Point out each Plasmodium parasite.
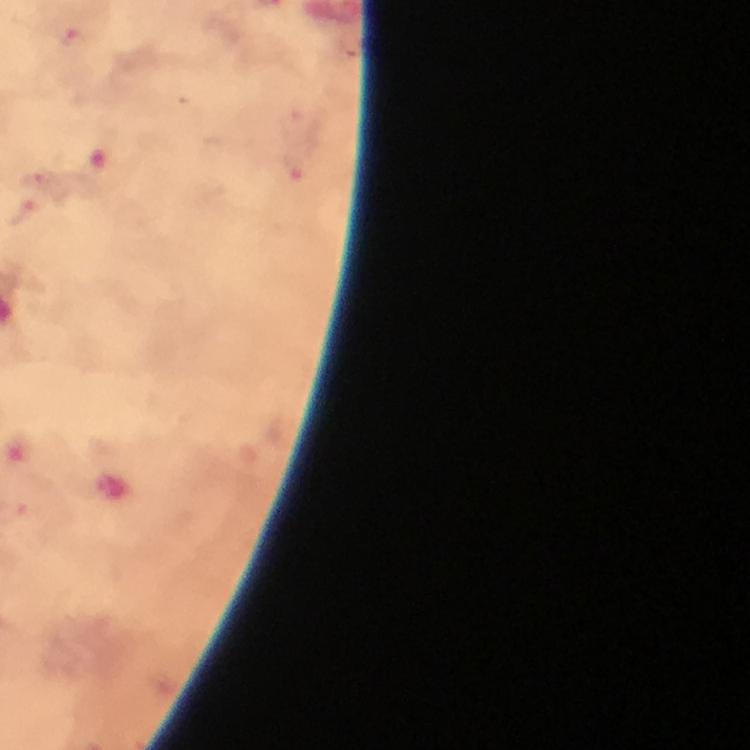
Approximate object centers, in pixels from the top-left corner.
Plasmodium parasites: (x=41, y=179), (x=23, y=213).

Photographed with a smartphone mounted on the microscope. Image is 750×750 pixels. Immersion oil applied. Thick blood film. Cropped region of a single field of view. At 100x magnification. Giemsa stain. From a diagnostic examination for malaria.